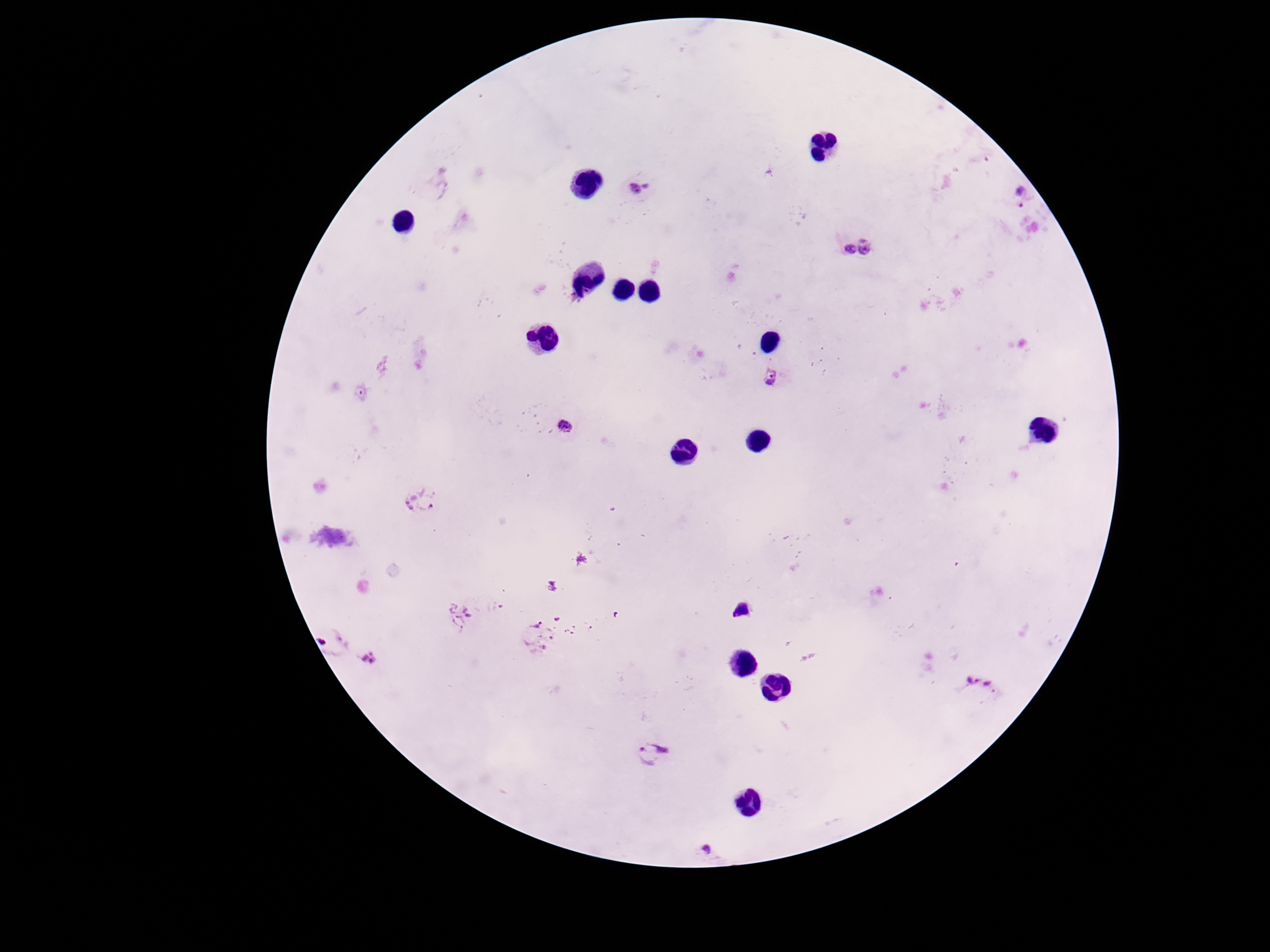
Approximate centers as [x, y] in pixels. Plasmodium parasite locations: [638, 188], [1015, 194], [869, 247], [846, 250], [773, 379], [565, 428], [419, 499], [459, 618], [537, 637], [329, 641], [372, 659], [980, 686], [653, 753], [709, 850]. 100x magnification. Patient malaria status: positive. Giemsa-stained preparation. Smartphone photograph taken through the microscope eyepiece. Image is 1270×952 pixels. One field from this slide. Thick blood smear.